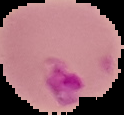

{
  "image_type": "cell region segmented out of the field of view; surrounding area masked to black",
  "preparation": "thin blood film",
  "image_size": "124×115 pixels",
  "malaria_status": "parasitized"
}